Describe the morphology of the red blood cells.
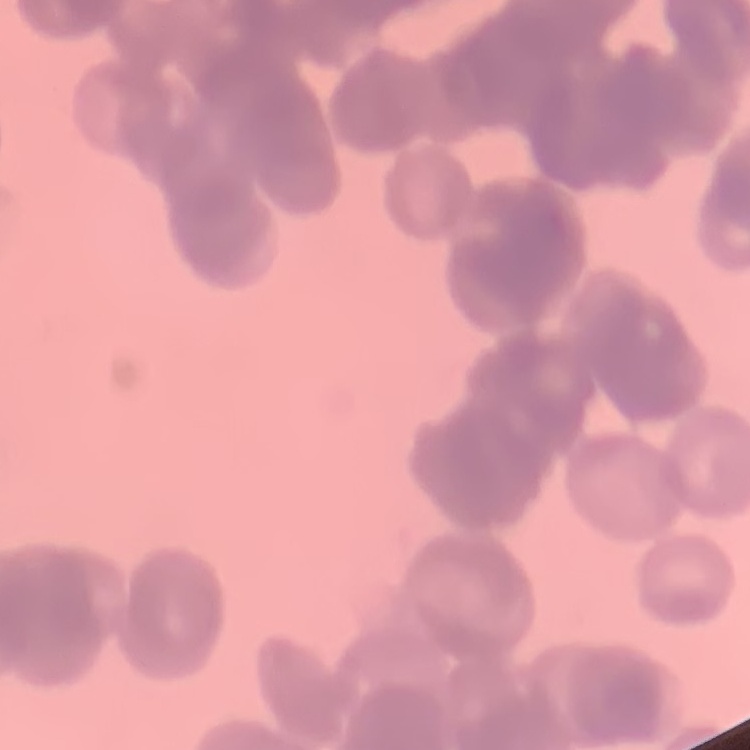

Rouleaux formation.

preparation = thin blood film
image type = square crop of a larger photomicrograph
stain = Field's or Giemsa